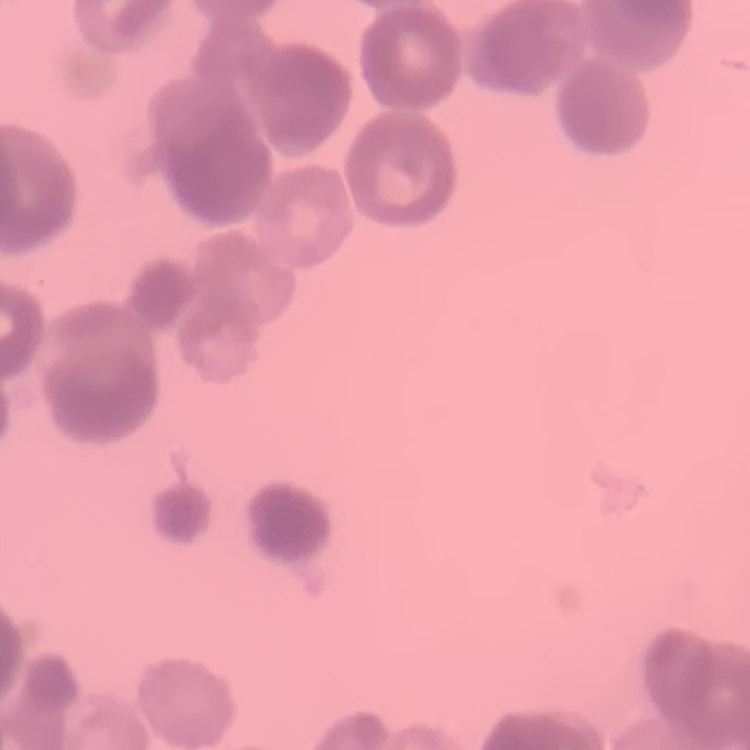

{
  "erythrocyte_morphology": "rouleaux formation",
  "stain": "Field's or Giemsa",
  "image_type": "square crop of a larger photomicrograph",
  "preparation": "thin peripheral smear"
}